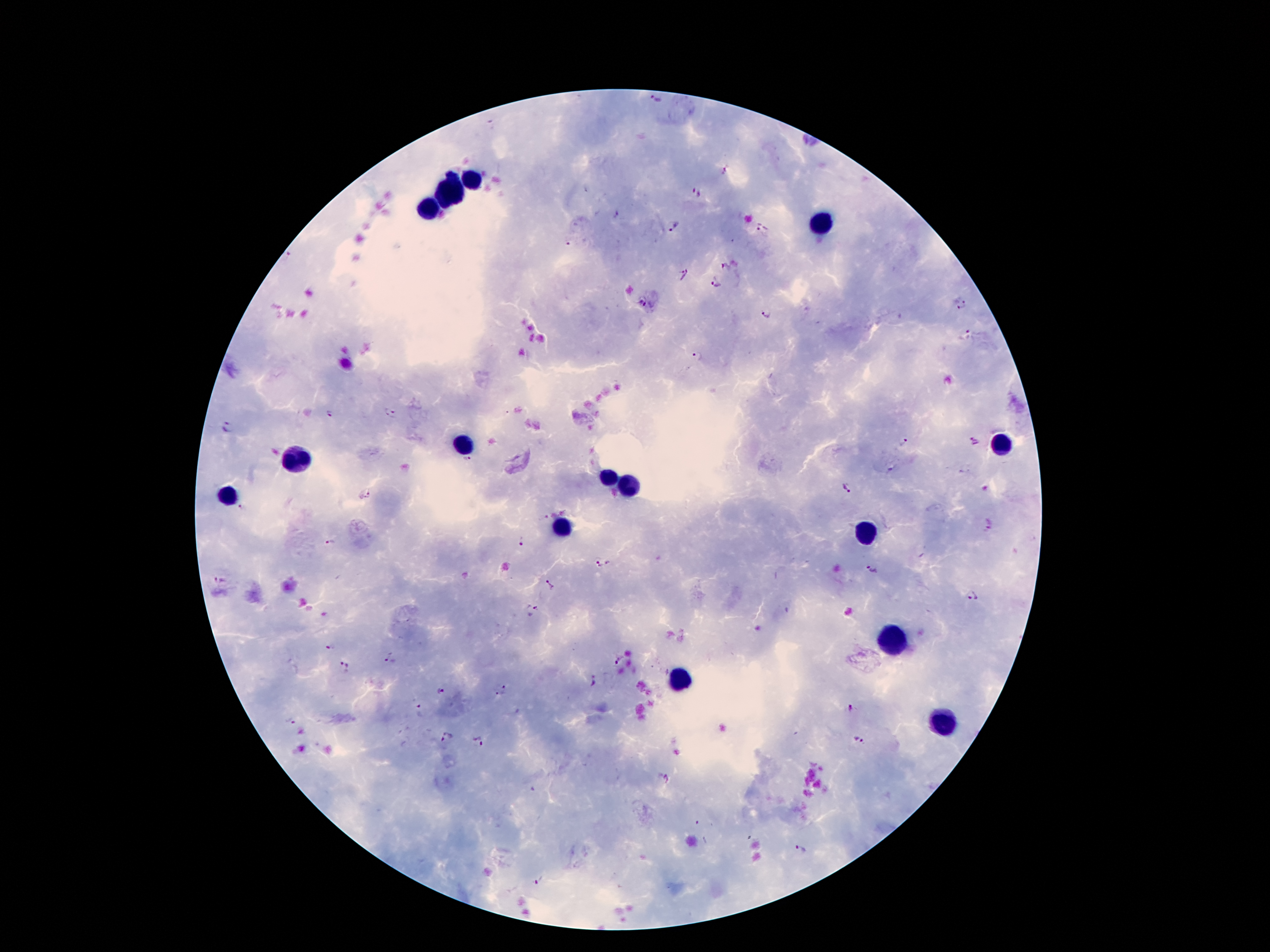

Approximate object centers, in pixels from the top-left corner.
Summary:
  - Leukocyte locations: (x=471, y=179), (x=451, y=193), (x=430, y=208), (x=822, y=224), (x=462, y=444), (x=1002, y=445), (x=299, y=461), (x=609, y=480), (x=628, y=488), (x=229, y=496), (x=562, y=527), (x=867, y=533), (x=891, y=643), (x=677, y=681), (x=945, y=721)
  - Malaria parasite locations: (x=655, y=100), (x=725, y=170), (x=697, y=193), (x=617, y=214), (x=671, y=226), (x=762, y=227), (x=567, y=246), (x=291, y=257), (x=724, y=267), (x=685, y=274), (x=714, y=283), (x=641, y=301), (x=961, y=306), (x=767, y=315), (x=967, y=332), (x=698, y=355), (x=330, y=414), (x=392, y=415), (x=226, y=428), (x=974, y=439), (x=904, y=441), (x=467, y=462), (x=848, y=489), (x=365, y=494), (x=242, y=506), (x=545, y=518), (x=990, y=528), (x=522, y=541), (x=330, y=542), (x=603, y=564), (x=873, y=570), (x=220, y=579), (x=549, y=585), (x=972, y=596), (x=532, y=608), (x=330, y=648), (x=386, y=655), (x=620, y=659), (x=343, y=661), (x=596, y=681), (x=503, y=685), (x=441, y=692), (x=500, y=694), (x=419, y=707), (x=849, y=708), (x=290, y=721), (x=447, y=737), (x=860, y=741), (x=478, y=742), (x=665, y=779), (x=800, y=850), (x=538, y=881)
  - Magnification: 100x
  - Patient malaria status: positive for Plasmodium falciparum
  - Stain: Giemsa
  - Preparation: thick peripheral-blood smear
  - Field of view: single
  - Capture: smartphone through the microscope eyepiece
  - Image size: 1270×952 pixels